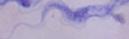 Micrograph. A trypanosome is seen. 1000x magnification.